State which parasite is depicted.
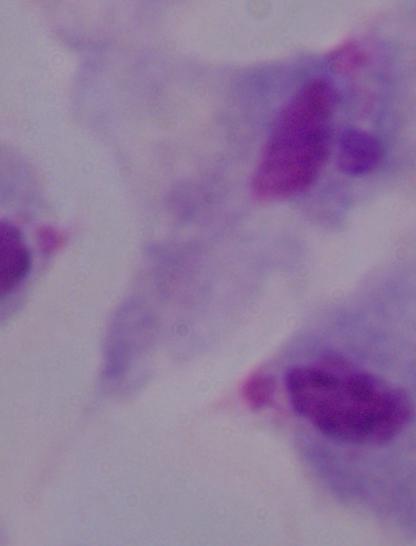
A trichomonad.

1000x magnification. Photomicrograph.